Classify this cell by malaria status.
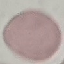
It is uninfected.

Automatically extracted cell patch, resized to 64 × 64 pixels. Giemsa stain. Acquired by smartphone through the microscope eyepiece. Thin blood smear.